Classify this cell by malaria status.
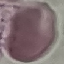
Uninfected.

Summary:
  - Stain: Giemsa
  - Preparation: thin smear
  - Image type: automatically extracted cell patch, resized to 64 × 64 pixels
  - Capture: smartphone through the microscope eyepiece